Identify the cell.
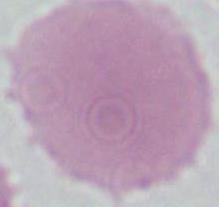
An erythrocyte.

Summary:
  - Magnification: 1000x
  - Modality: photomicrograph